Give the extent of all white blood cells.
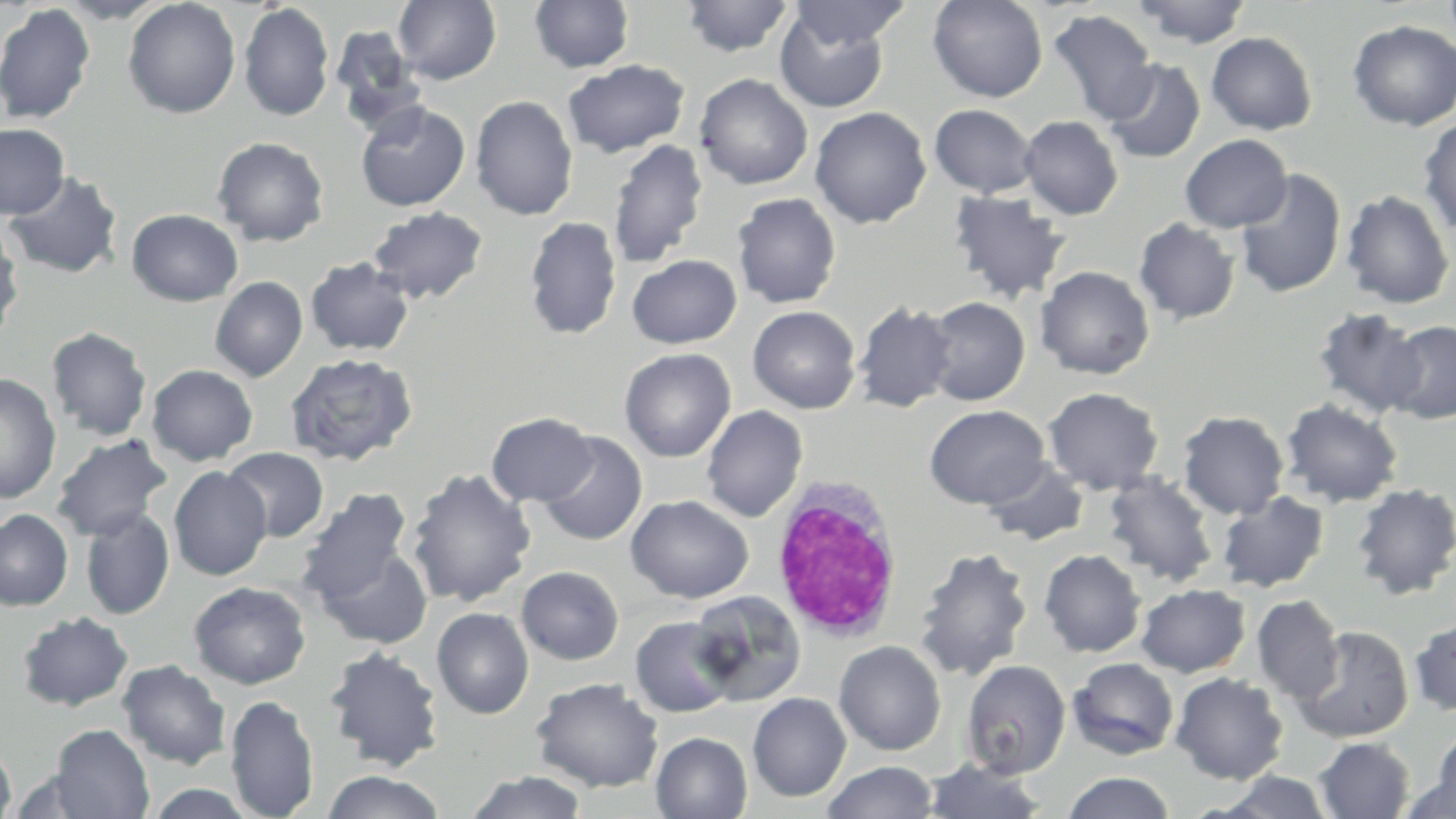

Approximate bounding boxes as [x1, y1, x2, y2] in pixels.
White blood cells: [770, 476, 905, 641].

Summary:
  - Uninfected red blood cell locations: [54, 0, 170, 23], [122, 0, 241, 118], [393, 0, 502, 85], [680, 0, 794, 57], [790, 0, 911, 50], [928, 0, 1048, 102], [1131, 0, 1252, 48], [529, 1, 635, 73], [0, 3, 96, 124], [238, 3, 334, 121], [775, 8, 889, 113], [1047, 9, 1159, 124], [1347, 20, 1456, 131], [329, 23, 425, 127], [1206, 32, 1317, 135], [1101, 58, 1206, 163], [562, 59, 690, 157], [694, 73, 813, 190], [470, 95, 579, 220], [355, 100, 471, 212], [929, 104, 1037, 198], [809, 107, 931, 228], [1019, 115, 1123, 220], [1418, 117, 1456, 237], [0, 123, 69, 219], [1179, 134, 1292, 233], [212, 136, 329, 247], [607, 139, 709, 269], [1235, 169, 1347, 299], [4, 170, 123, 279], [948, 190, 1071, 304], [1341, 190, 1454, 309], [732, 192, 841, 308], [367, 206, 488, 304], [127, 208, 243, 306], [524, 216, 622, 339], [1134, 218, 1240, 325], [0, 221, 23, 340], [627, 253, 741, 349], [305, 256, 414, 356], [1035, 265, 1155, 380], [210, 276, 308, 382], [922, 297, 1030, 406], [852, 302, 957, 413], [748, 305, 861, 414], [1313, 308, 1428, 418], [1383, 320, 1456, 423], [46, 326, 152, 442], [619, 348, 737, 462], [284, 352, 419, 466], [146, 364, 258, 466], [0, 373, 62, 505], [1043, 387, 1164, 494], [1281, 399, 1403, 508], [924, 405, 1050, 509], [701, 406, 808, 522], [1178, 411, 1289, 519], [487, 412, 597, 506], [538, 432, 648, 546], [51, 434, 172, 541], [222, 447, 329, 542], [980, 460, 1090, 547], [169, 466, 272, 581], [406, 468, 537, 608], [1102, 472, 1218, 588], [1351, 482, 1456, 600], [296, 488, 414, 606], [1217, 491, 1330, 593], [626, 495, 753, 604], [80, 507, 175, 619], [0, 508, 73, 611], [314, 543, 433, 649], [914, 546, 1033, 681], [1039, 549, 1146, 657], [516, 566, 624, 665], [189, 581, 311, 689], [1136, 583, 1250, 677], [688, 590, 807, 707], [1252, 594, 1344, 705], [432, 607, 534, 719], [17, 611, 134, 712], [1409, 615, 1456, 716], [630, 616, 739, 717], [1294, 625, 1414, 743], [834, 640, 946, 755], [323, 645, 445, 772], [1068, 657, 1179, 759], [117, 659, 232, 770], [961, 659, 1071, 779], [1170, 672, 1288, 784], [531, 677, 664, 793], [748, 692, 851, 801], [226, 694, 319, 818], [49, 725, 154, 819], [651, 732, 752, 818], [1427, 732, 1456, 818], [1314, 737, 1415, 818], [0, 740, 16, 819], [923, 759, 1049, 819], [823, 761, 938, 818], [6, 768, 104, 818], [465, 770, 588, 819], [322, 771, 446, 818], [1061, 771, 1176, 819], [1215, 771, 1335, 818], [1402, 771, 1455, 819], [144, 784, 259, 818]
  - Slide-level diagnosis: negative for blood parasites
  - Field of view: single
  - Image size: 1456×819 pixels
  - Modality: optical microscopy
  - Stain: May-Grünwald-Giemsa
  - Preparation: thin blood film
  - Magnification: 1000x